State which parasite is depicted.
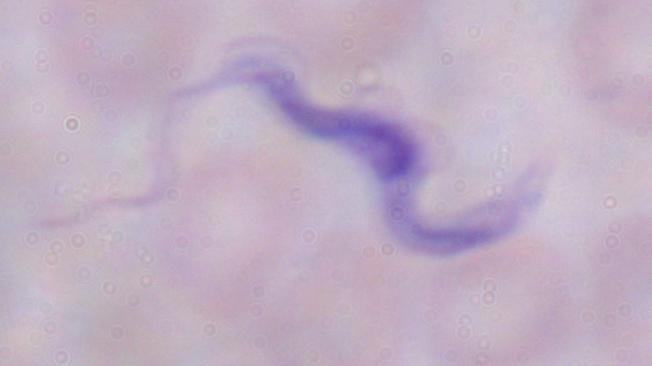
This is a trypanosome.

Summary:
  - Magnification: 1000x
  - Modality: micrograph